Assess this cell for malaria.
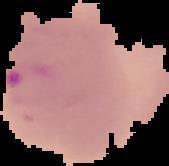
It is parasitized.

image type = segmented cell region with the area outside set to black
image size = 169×166 pixels
preparation = thin blood film